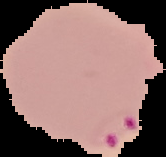

Image is 166×157 pixels. Result: Plasmodium parasites detected. Cell region segmented out of the field of view; the surrounding area is masked to black. From a thin blood film.